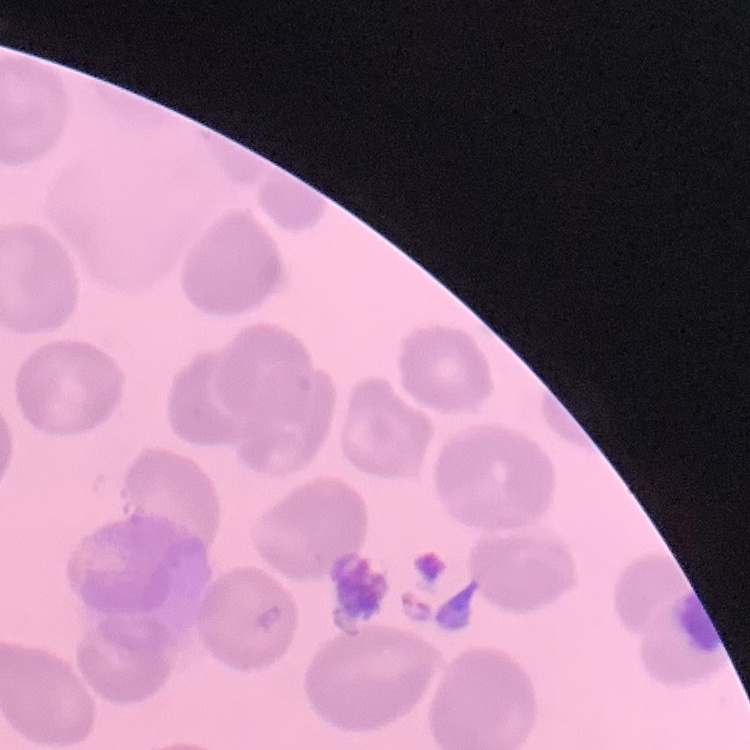

The erythrocytes exhibit no rouleaux formation. Field's or Giemsa stain. Thin peripheral smear. One tile cut from a larger photomicrograph.